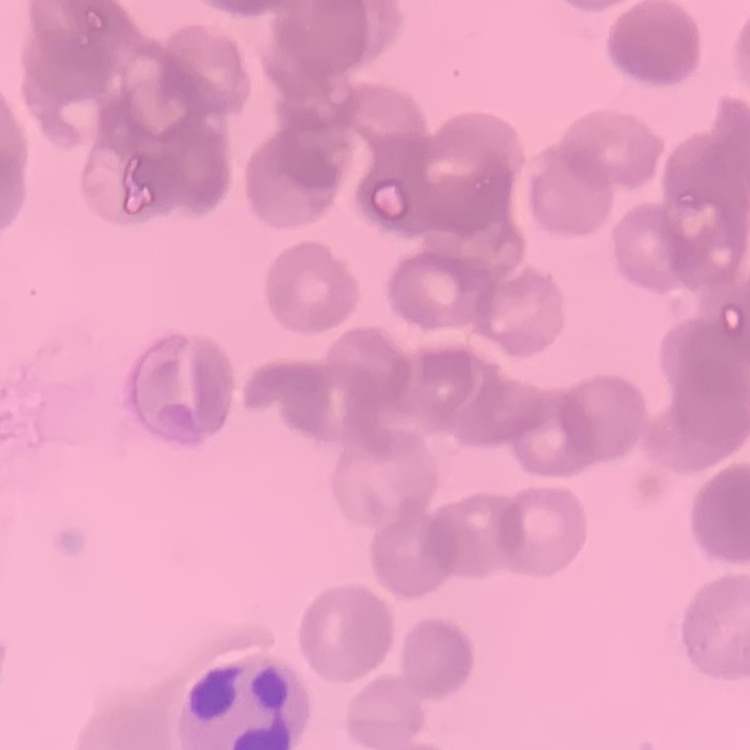

erythrocyte_morphology: rouleaux formation
preparation: thin blood film
image_type: one tile cut from a larger photomicrograph
stain: Field's or Giemsa